Classify this cell by malaria status.
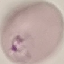

It is parasitized.

capture: smartphone camera at the microscope eyepiece
preparation: thin blood film
image_type: cell patch, automatically extracted from a larger field of view and resized to 64 × 64 pixels
stain: Giemsa